Assess this cell for malaria.
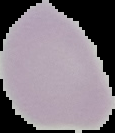

Uninfected.

Summary:
  - Preparation: thin blood film
  - Image type: segmented cell region with the area outside set to black
  - Image size: 115×133 pixels